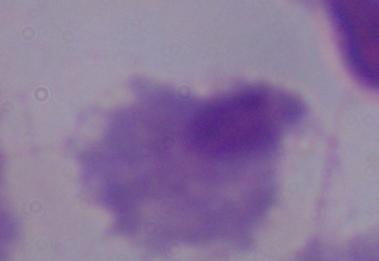

identification: trichomonad
modality: micrograph
magnification: 1000x